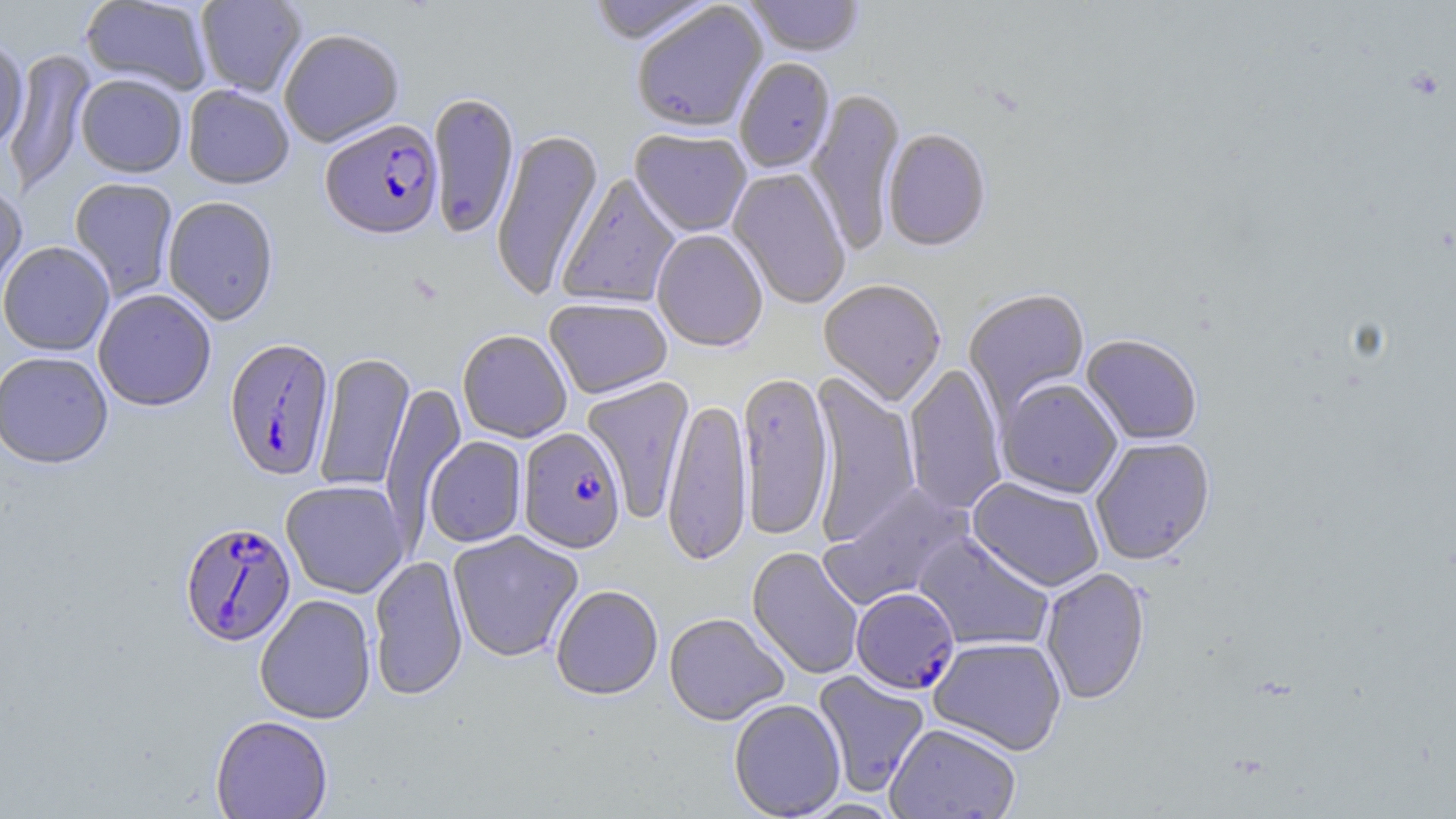
Approximate bounding boxes as [x1, y1, x2, y2] in pixels. Uninfected red blood cell locations: [81, 0, 212, 95], [195, 0, 308, 98], [585, 0, 717, 47], [743, 0, 866, 59], [632, 5, 769, 135], [279, 30, 405, 148], [0, 40, 29, 152], [4, 50, 96, 195], [735, 59, 836, 175], [76, 75, 187, 178], [183, 85, 294, 190], [806, 89, 906, 256], [428, 93, 520, 241], [490, 129, 605, 300], [629, 131, 751, 238], [883, 131, 992, 254], [728, 169, 851, 310], [557, 174, 680, 309], [69, 178, 179, 302], [0, 183, 28, 306], [163, 196, 279, 326], [652, 231, 768, 353], [0, 242, 114, 357], [818, 281, 946, 407], [93, 289, 216, 412], [963, 290, 1090, 417], [544, 299, 672, 400], [457, 330, 572, 443], [1081, 335, 1202, 446], [0, 351, 114, 470], [314, 352, 415, 493], [903, 363, 1008, 516], [737, 373, 834, 542], [808, 373, 921, 545], [582, 377, 695, 524], [997, 380, 1122, 499], [380, 382, 466, 544], [662, 397, 752, 569], [425, 437, 527, 548], [1091, 438, 1216, 566], [968, 477, 1104, 593], [281, 480, 409, 598], [820, 483, 973, 610], [447, 531, 583, 663], [915, 532, 1053, 652], [747, 547, 863, 680], [369, 555, 468, 701], [1041, 567, 1151, 705], [551, 585, 663, 702], [254, 594, 377, 724], [664, 613, 789, 726], [928, 637, 1067, 756], [812, 670, 930, 798], [728, 698, 846, 819], [210, 715, 333, 818], [884, 724, 1021, 819]. Plasmodium falciparum-infected red blood cell locations: [321, 122, 443, 242], [224, 338, 335, 482], [518, 427, 626, 555], [180, 521, 296, 647], [851, 588, 960, 696]. Slide-level diagnosis: Plasmodium falciparum. Image is 1456×819 pixels. Optical microscopy. May-Grünwald-Giemsa-stained preparation. Captured at 1000x magnification. Thin blood smear. Single field of view.